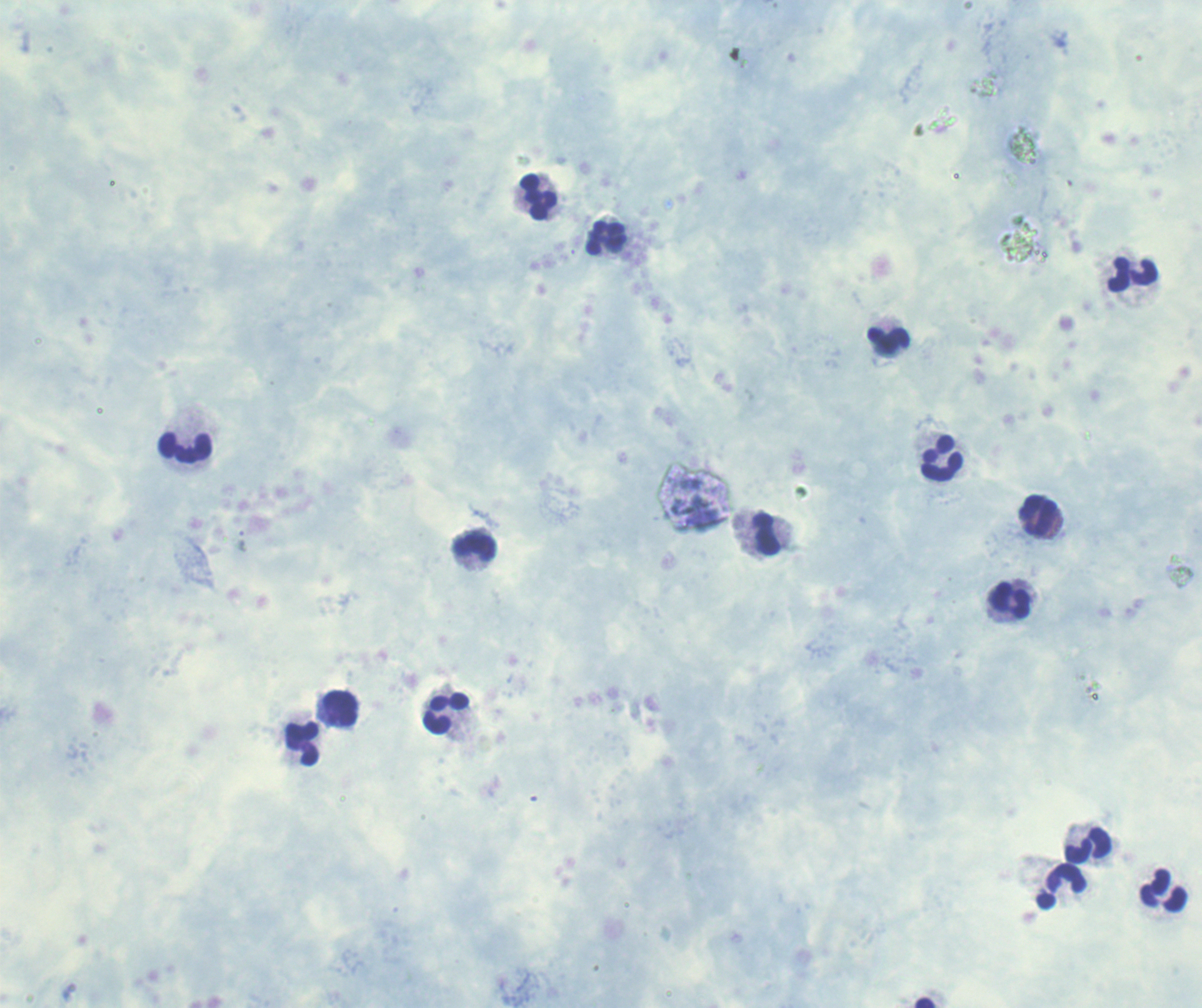

coordinate format = approximate object centers, in pixels from the top-left corner
leukocyte locations = (x=539, y=198), (x=607, y=239), (x=1133, y=275), (x=888, y=340), (x=185, y=448), (x=942, y=460), (x=1039, y=517), (x=767, y=534), (x=475, y=548), (x=1011, y=601), (x=341, y=709), (x=446, y=715), (x=303, y=744), (x=1088, y=846), (x=1062, y=887), (x=1165, y=892), (x=926, y=1002)
result = no malaria parasites seen
magnification = 100x
context = previously used in an actual diagnosis
preparation = thick blood smear
stain = Romanowsky
field of view = single
image size = 1202×1008 pixels
background quality = unsatisfactory